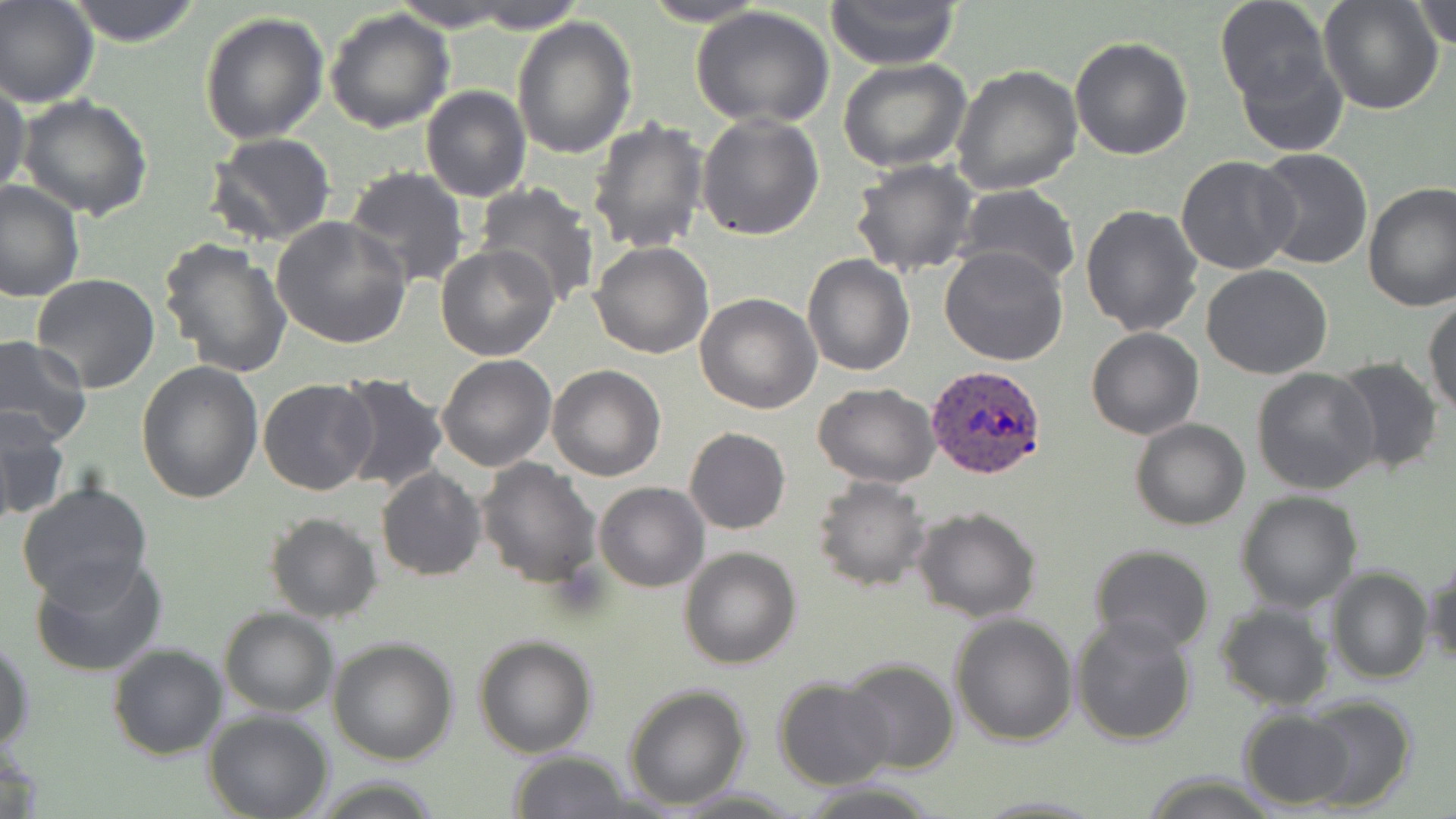

Approximate bounding boxes as named x1/y1/x2/y2 corners in pixels. Uninfected red blood cell locations: (x1=0, y1=0, x2=97, y2=107), (x1=67, y1=0, x2=203, y2=46), (x1=391, y1=0, x2=520, y2=32), (x1=463, y1=0, x2=586, y2=34), (x1=640, y1=0, x2=771, y2=27), (x1=826, y1=0, x2=963, y2=69), (x1=1215, y1=0, x2=1331, y2=108), (x1=1317, y1=1, x2=1443, y2=114), (x1=1412, y1=1, x2=1456, y2=51), (x1=692, y1=7, x2=837, y2=128), (x1=325, y1=9, x2=456, y2=133), (x1=199, y1=10, x2=329, y2=144), (x1=512, y1=17, x2=638, y2=160), (x1=1069, y1=34, x2=1193, y2=159), (x1=1237, y1=43, x2=1350, y2=158), (x1=837, y1=58, x2=970, y2=170), (x1=950, y1=64, x2=1081, y2=195), (x1=0, y1=82, x2=31, y2=199), (x1=421, y1=86, x2=531, y2=201), (x1=17, y1=95, x2=154, y2=221), (x1=696, y1=112, x2=824, y2=241), (x1=587, y1=118, x2=709, y2=253), (x1=206, y1=133, x2=337, y2=246), (x1=1253, y1=148, x2=1374, y2=271), (x1=1176, y1=155, x2=1300, y2=275), (x1=850, y1=159, x2=979, y2=278), (x1=344, y1=166, x2=469, y2=290), (x1=0, y1=179, x2=83, y2=303), (x1=1362, y1=182, x2=1456, y2=311), (x1=472, y1=185, x2=599, y2=306), (x1=955, y1=186, x2=1081, y2=293), (x1=1078, y1=203, x2=1204, y2=339), (x1=270, y1=217, x2=413, y2=348), (x1=158, y1=237, x2=293, y2=377), (x1=588, y1=241, x2=714, y2=359), (x1=435, y1=244, x2=559, y2=362), (x1=940, y1=246, x2=1071, y2=366), (x1=803, y1=253, x2=914, y2=377), (x1=1201, y1=265, x2=1333, y2=380), (x1=30, y1=273, x2=159, y2=394), (x1=695, y1=292, x2=821, y2=413), (x1=1424, y1=294, x2=1456, y2=419), (x1=1086, y1=328, x2=1203, y2=440), (x1=0, y1=336, x2=92, y2=446), (x1=436, y1=355, x2=556, y2=473), (x1=1330, y1=357, x2=1445, y2=477), (x1=137, y1=361, x2=265, y2=504), (x1=548, y1=364, x2=666, y2=481), (x1=1252, y1=369, x2=1379, y2=495), (x1=334, y1=373, x2=450, y2=496), (x1=258, y1=378, x2=378, y2=496), (x1=812, y1=382, x2=939, y2=488), (x1=1, y1=405, x2=70, y2=520), (x1=1130, y1=418, x2=1250, y2=531), (x1=684, y1=427, x2=790, y2=534), (x1=476, y1=458, x2=602, y2=590), (x1=376, y1=468, x2=487, y2=581), (x1=812, y1=475, x2=930, y2=591), (x1=594, y1=481, x2=708, y2=591), (x1=15, y1=482, x2=153, y2=604), (x1=1235, y1=490, x2=1361, y2=611), (x1=912, y1=507, x2=1041, y2=623), (x1=265, y1=511, x2=381, y2=624), (x1=679, y1=545, x2=801, y2=668), (x1=1089, y1=545, x2=1215, y2=655), (x1=1424, y1=552, x2=1456, y2=669), (x1=30, y1=553, x2=168, y2=678), (x1=1327, y1=567, x2=1433, y2=684), (x1=1215, y1=602, x2=1333, y2=711), (x1=218, y1=608, x2=337, y2=716), (x1=950, y1=612, x2=1078, y2=744), (x1=1070, y1=613, x2=1197, y2=745), (x1=0, y1=632, x2=35, y2=756), (x1=473, y1=634, x2=597, y2=758), (x1=328, y1=637, x2=459, y2=763), (x1=106, y1=642, x2=228, y2=761), (x1=841, y1=658, x2=959, y2=772), (x1=773, y1=677, x2=896, y2=789), (x1=623, y1=686, x2=750, y2=810), (x1=1299, y1=695, x2=1417, y2=811), (x1=1238, y1=708, x2=1353, y2=808), (x1=205, y1=710, x2=333, y2=819), (x1=508, y1=751, x2=633, y2=818), (x1=1142, y1=775, x2=1283, y2=818), (x1=795, y1=781, x2=939, y2=818). Plasmodium ovale-infected red blood cell locations: (x1=927, y1=364, x2=1047, y2=479). Slide-level diagnosis: Plasmodium ovale. Thin blood film. May-Grünwald-Giemsa-stained preparation. Image is 1456×819 pixels. 1000x magnification. Light microscopy. One field of a larger specimen.